Report the malaria status of this cell.
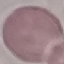
Uninfected.

Automatically extracted cell patch, resized to 64 × 64 pixels. Giemsa-stained preparation. Acquired by smartphone through the microscope eyepiece. Thin smear of blood.